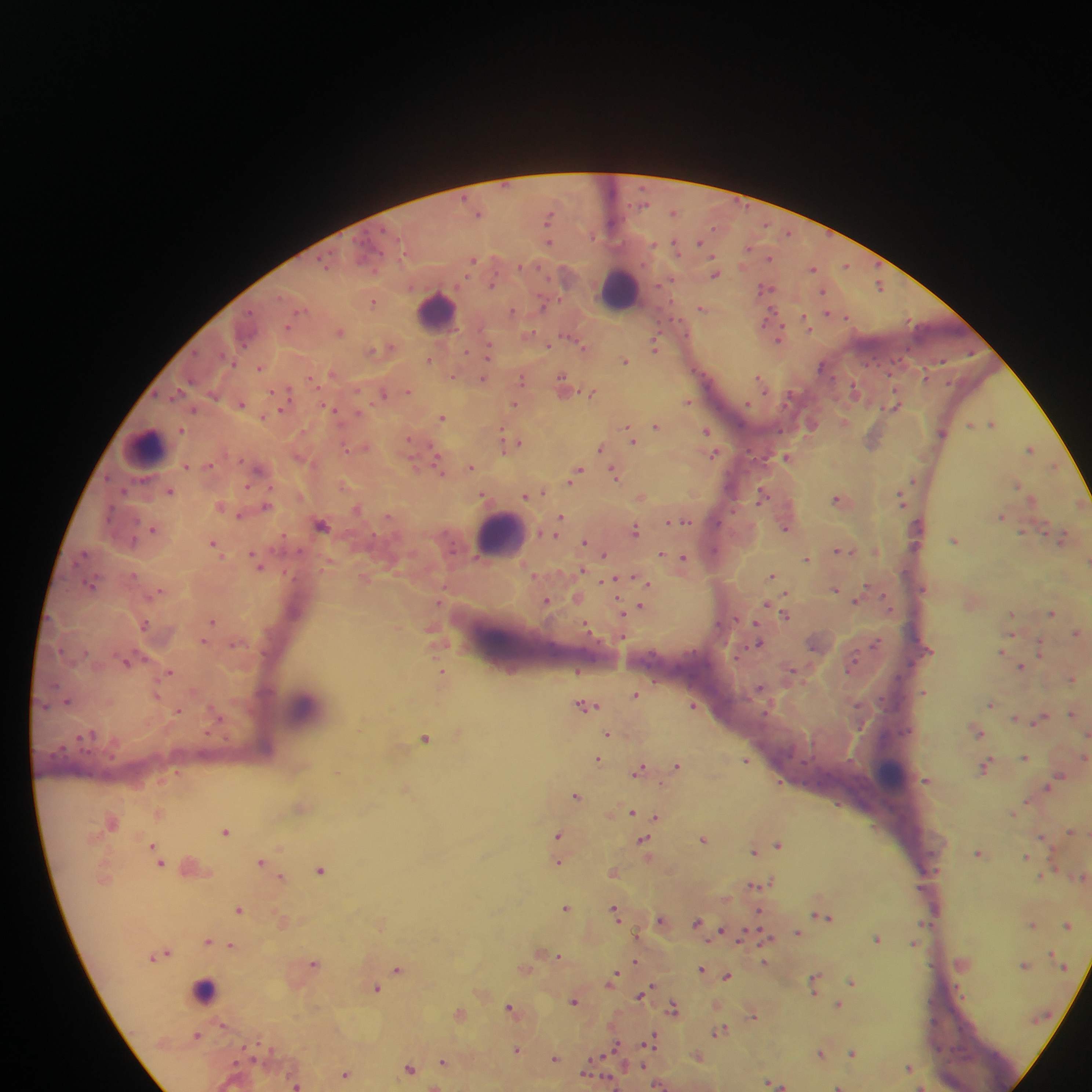

Approximate centers as x y in pixels. Plasmodium parasite locations: 674 212; 478 213; 549 216; 612 222; 789 233; 701 241; 548 242; 675 244; 653 245; 749 247; 770 259; 473 261; 324 264; 846 265; 520 266; 813 268; 716 274; 492 283; 880 286; 764 288; 824 292; 374 301; 543 305; 302 309; 702 309; 513 310; 770 313; 827 313; 847 316; 766 320; 806 322; 340 331; 530 333; 780 337; 568 338; 578 342; 548 345; 582 346; 654 347; 388 348; 374 349; 489 349; 465 352; 430 360; 626 360; 822 366; 259 368; 331 374; 453 375; 926 377; 759 378; 191 379; 311 379; 484 379; 522 379; 562 381; 855 390; 409 391; 287 392; 383 393; 592 393; 688 401; 241 403; 515 403; 893 405; 193 410; 333 410; 280 411; 442 416; 844 422; 991 423; 656 425; 972 425; 812 426; 707 431; 941 432; 630 433; 409 440; 632 440; 872 441; 502 443; 519 443; 366 447; 1030 448; 347 449; 599 449; 714 454; 786 457; 436 458; 186 466; 471 467; 1053 467; 258 469; 439 469; 577 471; 615 473; 913 480; 1017 484; 170 492; 761 494; 526 495; 641 497; 901 498; 838 499; 1032 499; 266 506; 358 509; 109 515; 239 516; 388 516; 1002 516; 560 517; 683 521; 670 522; 322 525; 785 528; 153 529; 635 530; 1062 538; 955 540; 584 541; 213 543; 714 550; 842 551; 662 553; 604 554; 684 557; 807 559; 256 561; 582 570; 771 575; 635 577; 610 581; 644 581; 90 584; 867 587; 835 588; 546 601; 856 601; 767 604; 641 606; 621 612; 1052 613; 786 615; 212 621; 144 625; 588 626; 757 627; 1077 633; 202 641; 758 642; 875 644; 1040 648; 1003 651; 126 662; 851 665; 1021 667; 170 672; 442 672; 792 673; 1072 678; 760 689; 924 692; 635 695; 157 696; 68 701; 991 704; 693 705; 586 706; 178 711; 1071 713; 1016 718; 1041 718; 977 732; 608 734; 425 738; 1025 757; 599 759; 745 761; 676 766; 986 766; 639 769; 1059 777; 926 780; 1049 786; 576 795; 633 812; 656 817; 225 831; 558 835; 1043 837; 703 839; 644 841; 778 845; 152 846; 754 851; 979 853; 1026 856; 260 862; 160 863; 558 863; 320 870; 613 872; 281 877; 755 885; 566 907; 238 910; 615 911; 825 917; 660 919; 697 923; 1067 924; 1033 925; 721 931; 798 933; 742 937; 767 938; 877 939; 208 941; 913 944; 232 946; 167 952; 558 956; 635 961; 314 962; 765 962; 1025 965; 702 969; 397 970; 727 976; 614 977; 852 982; 815 983; 376 988; 642 994; 574 1001; 839 1004; 510 1007; 674 1008; 460 1014; 753 1015; 719 1031; 197 1035; 652 1041; 616 1048; 517 1050; 852 1053; 820 1054; 555 1058; 443 1062; 908 1067; 410 1068; 345 1074; 772 1082; 295 1085; 659 1085; 839 1086; 922 1086. Leukocyte locations: 620 289; 437 308; 145 447; 500 534; 304 707; 892 773; 209 990. Single field of view. Collected in Ghana. Mobile-phone photograph taken through the microscope. Thick blood film. Image is 1092×1092 pixels.